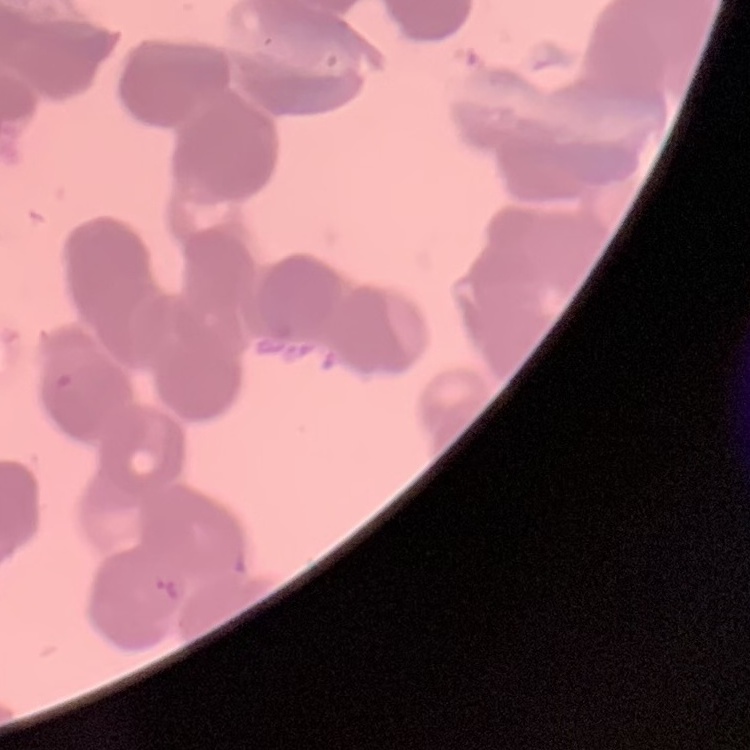
The red blood cells show rouleaux formation. One tile cut from a larger photomicrograph. Thin peripheral smear. Stained with either Field's or Giemsa.